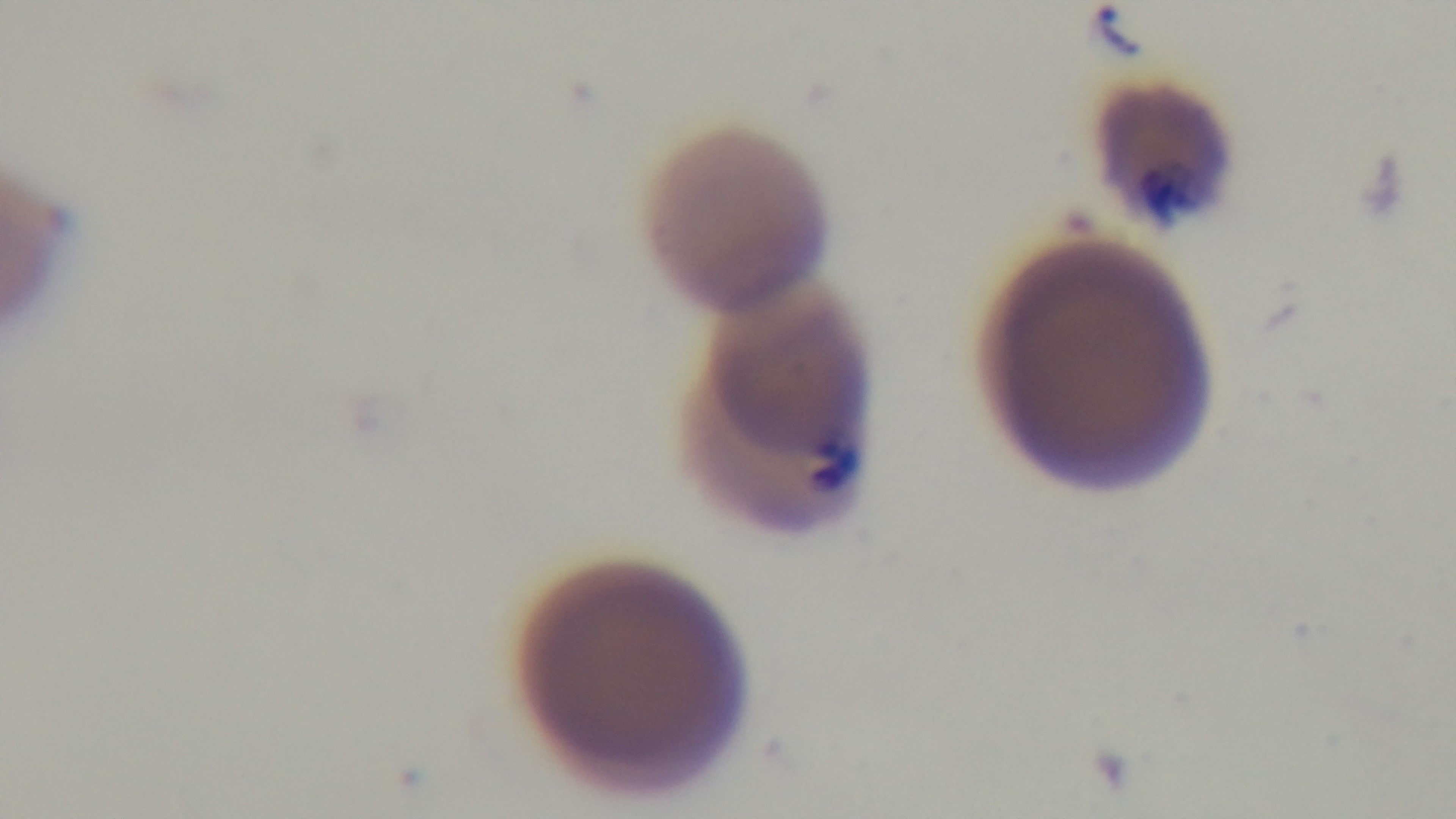

Malaria status: positive. One field from the slide. Preparation: thin. Captured with a mounted 4K digital camera. Giemsa-stained. Light microscopy. Oil-immersion objective, 100x.